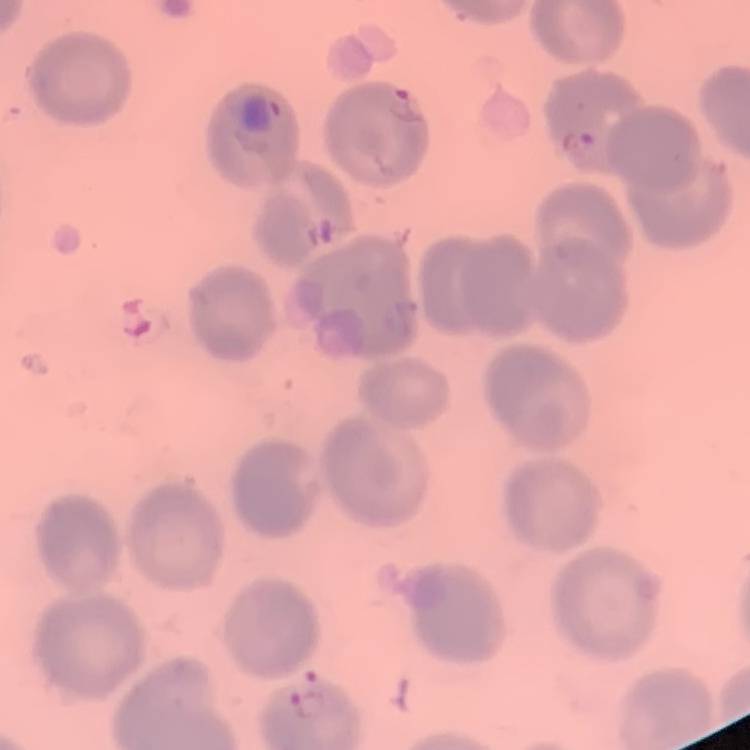
Summary:
  - Red blood cell morphology: no rouleaux formation
  - Image type: one tile cut from a larger photomicrograph
  - Stain: Field's or Giemsa
  - Preparation: thin blood film